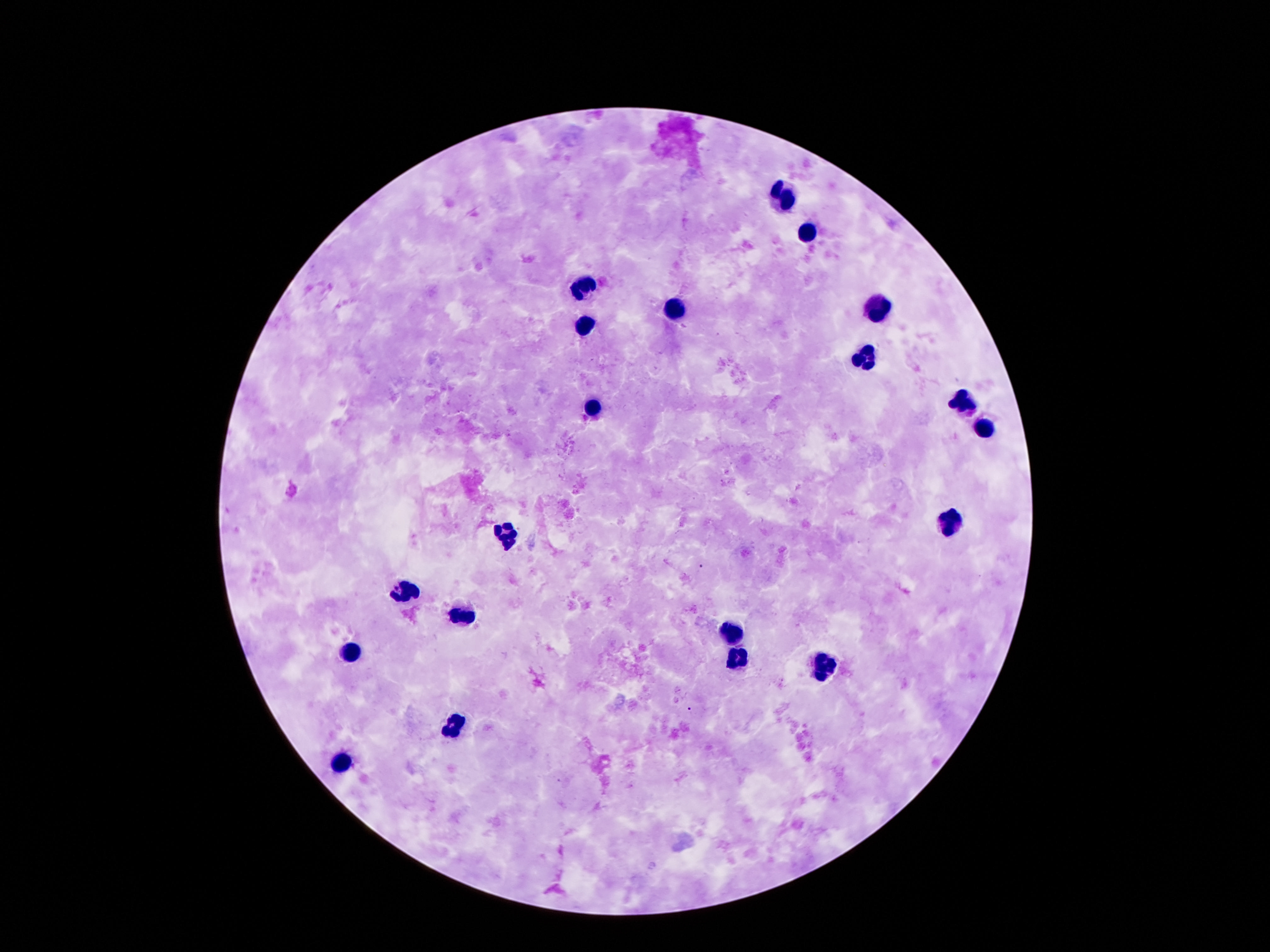
patient malaria status = uninfected
field of view = one from this slide
capture = smartphone camera through the microscope eyepiece
image size = 1270×952 pixels
magnification = 100x
preparation = thick blood film
stain = Giemsa
leukocyte locations = approximate centers as (x, y) in pixels: (783, 194), (806, 231), (584, 283), (879, 307), (675, 309), (586, 326), (866, 359), (964, 402), (594, 407), (985, 428), (951, 526), (505, 533), (405, 591), (463, 615), (732, 633), (350, 653), (736, 657), (824, 668), (455, 725), (340, 763)